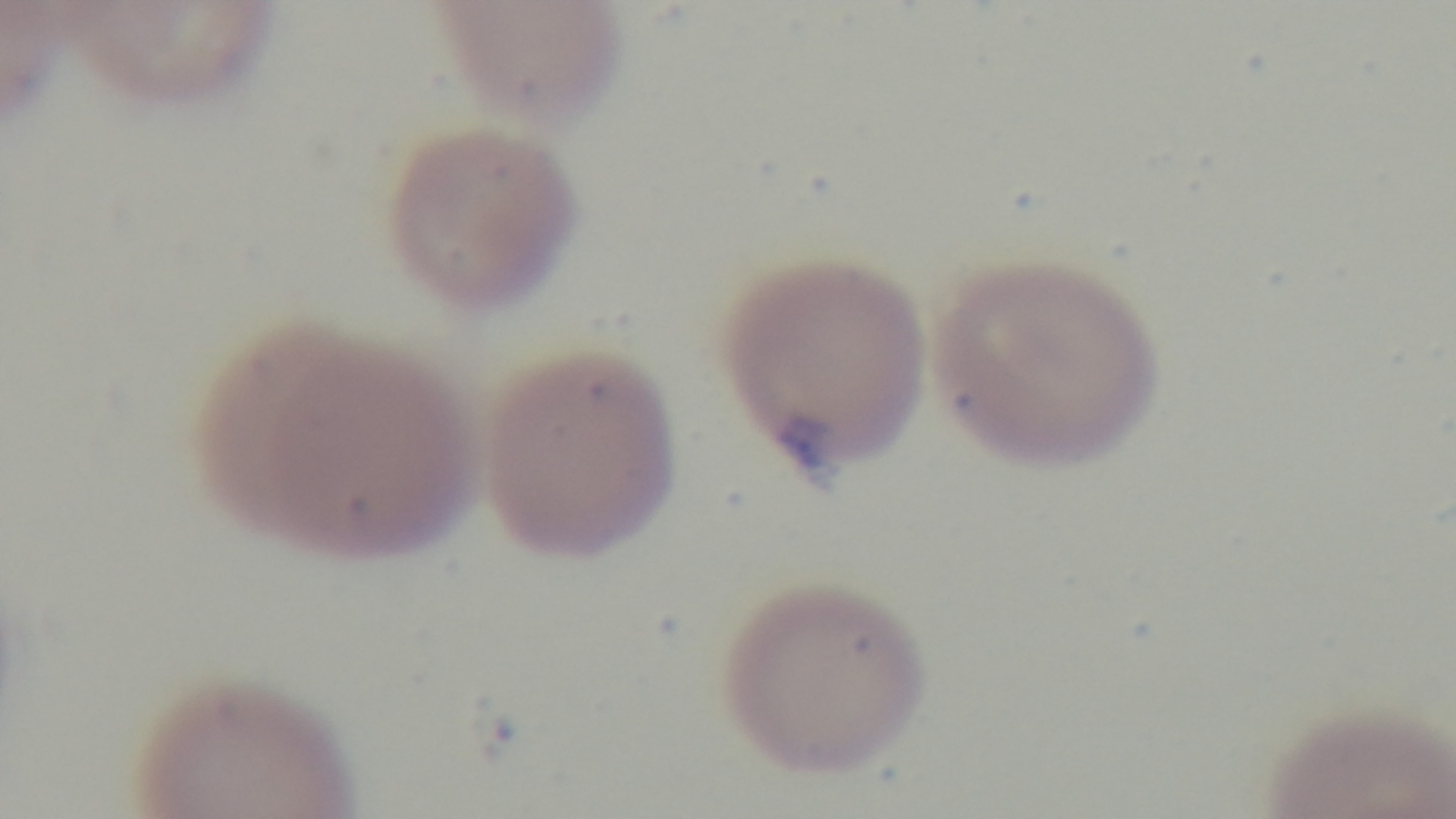

Summary:
  - Stain: Giemsa
  - Preparation: thin
  - Field of view: one from the slide
  - Malaria status: infected
  - Objective: 100x oil immersion
  - Capture: mounted 4K digital camera
  - Modality: light microscopy